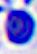
modality = photomicrograph
magnification = 400x
identification = leukocyte